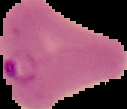
Summary:
  - Preparation: thin blood film
  - Image size: 127×109 pixels
  - Image type: segmented cell region on a black background
  - Malaria status: parasitized